Assess this cell for malaria.
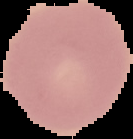

Uninfected.

image size = 133×139 pixels
image type = segmented cell region on a black background
preparation = thin blood film